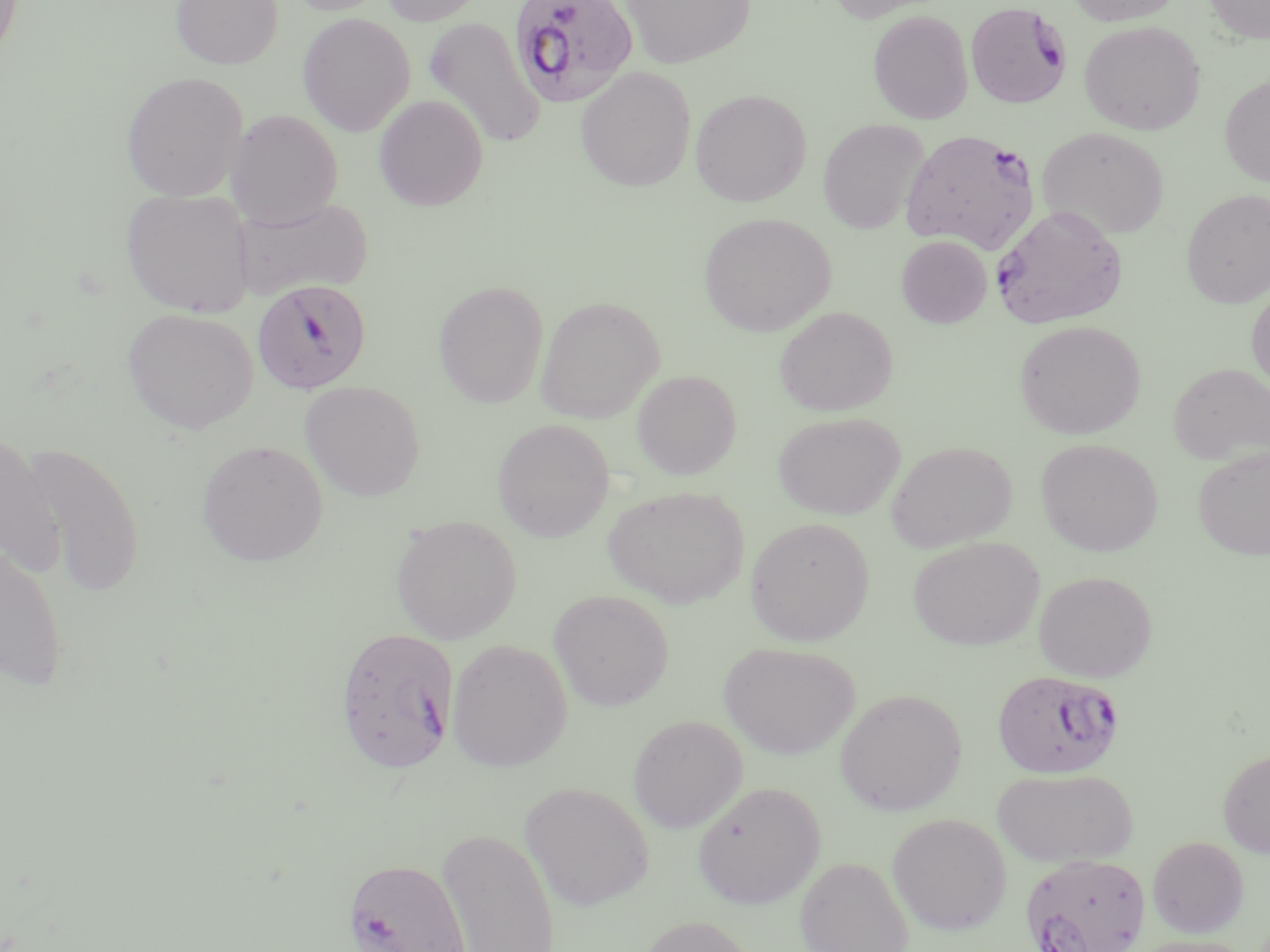

Summary:
  - Coordinate format: approximate bounding boxes as (x1, y1, x2, y2) in pixels
  - Uninfected red blood cell locations: (0, 0, 23, 64), (171, 0, 283, 69), (285, 0, 393, 16), (378, 0, 488, 26), (620, 0, 755, 68), (825, 0, 947, 22), (1064, 0, 1184, 26), (1204, 0, 1270, 44), (867, 10, 973, 125), (297, 13, 415, 136), (425, 17, 545, 149), (1079, 21, 1205, 135), (575, 67, 696, 192), (121, 71, 248, 201), (1220, 76, 1270, 187), (690, 88, 811, 206), (374, 95, 488, 211), (226, 109, 343, 228), (818, 119, 929, 234), (1038, 125, 1170, 240), (120, 188, 256, 316), (1182, 189, 1270, 307), (232, 194, 374, 302), (698, 213, 836, 336), (896, 235, 992, 328), (433, 281, 549, 407), (1247, 284, 1270, 394), (535, 296, 664, 423), (775, 306, 898, 417), (122, 308, 259, 435), (1014, 320, 1146, 439), (1168, 363, 1270, 466), (632, 369, 742, 480), (300, 381, 426, 501), (773, 412, 905, 520), (493, 418, 614, 542), (1, 434, 65, 577), (1036, 439, 1164, 556), (197, 440, 328, 566), (886, 440, 1017, 552), (18, 441, 146, 597), (1192, 447, 1270, 560), (602, 484, 749, 608), (391, 515, 522, 644), (745, 517, 874, 646), (907, 536, 1044, 651), (0, 537, 69, 692), (1033, 570, 1157, 683), (549, 590, 674, 710), (447, 639, 572, 772), (719, 641, 860, 759), (835, 689, 967, 815), (628, 714, 747, 833), (1218, 748, 1270, 858), (993, 768, 1138, 867), (521, 781, 654, 910), (692, 781, 825, 908), (888, 813, 1012, 935), (437, 827, 560, 951), (1148, 836, 1249, 938), (796, 856, 913, 952), (635, 915, 761, 952), (1125, 935, 1255, 952)
  - Plasmodium falciparum-infected red blood cell locations: (509, 0, 638, 108), (965, 2, 1072, 109), (901, 129, 1040, 253), (991, 205, 1128, 330), (252, 280, 372, 394), (334, 626, 460, 775), (992, 668, 1125, 780), (1021, 853, 1150, 952), (344, 857, 472, 952)
  - Slide-level diagnosis: Plasmodium falciparum
  - Preparation: thin blood smear
  - Modality: light microscopy
  - Magnification: 1000x
  - Stain: May-Grünwald-Giemsa
  - Field of view: single
  - Image size: 1270×952 pixels